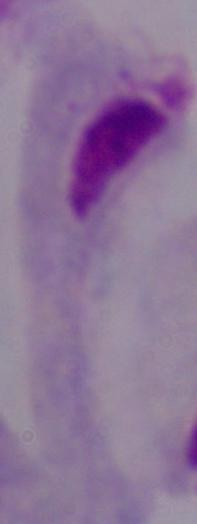
identification: trichomonad
magnification: 1000x
modality: micrograph